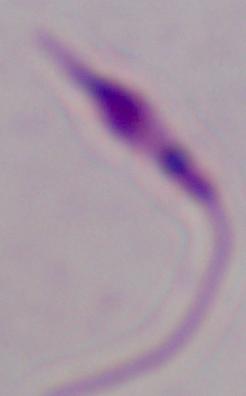
Summary:
  - Magnification: 1000x
  - Identification: Leishmania
  - Modality: micrograph